Assess this cell for malaria.
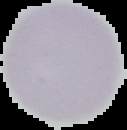
It is uninfected.

Summary:
  - Image size: 127×130 pixels
  - Image type: segmented cell region on a black background
  - Preparation: thin blood smear